Give the position of every malaria parasite.
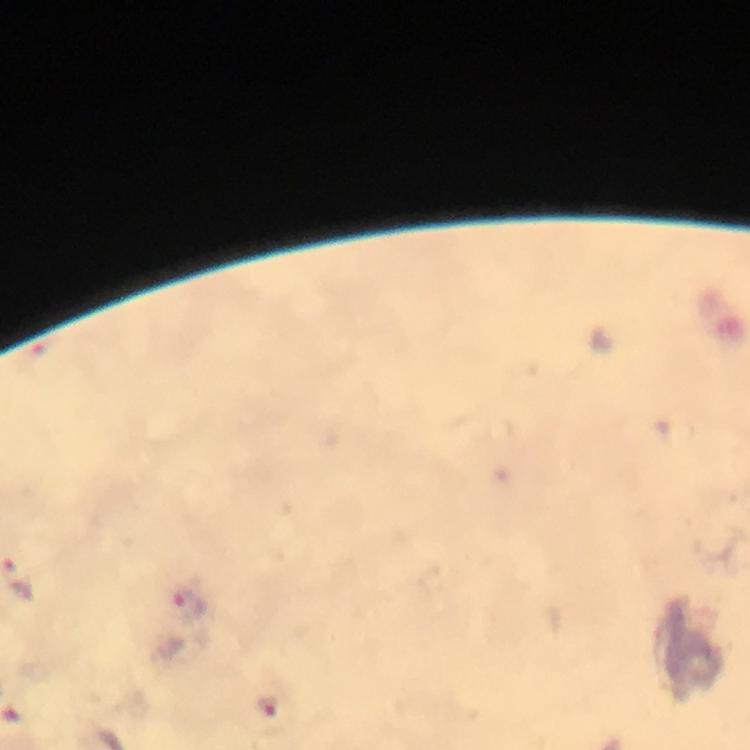
Approximate centers as [x, y] in pixels.
Malaria parasites: [187, 605], [265, 706].

preparation = thick blood smear
stain = Giemsa
immersion oil = used
magnification = 100x
image size = 750×750 pixels
cropped from = one field of view
context = from a diagnostic examination for malaria
capture = smartphone mounted on the microscope